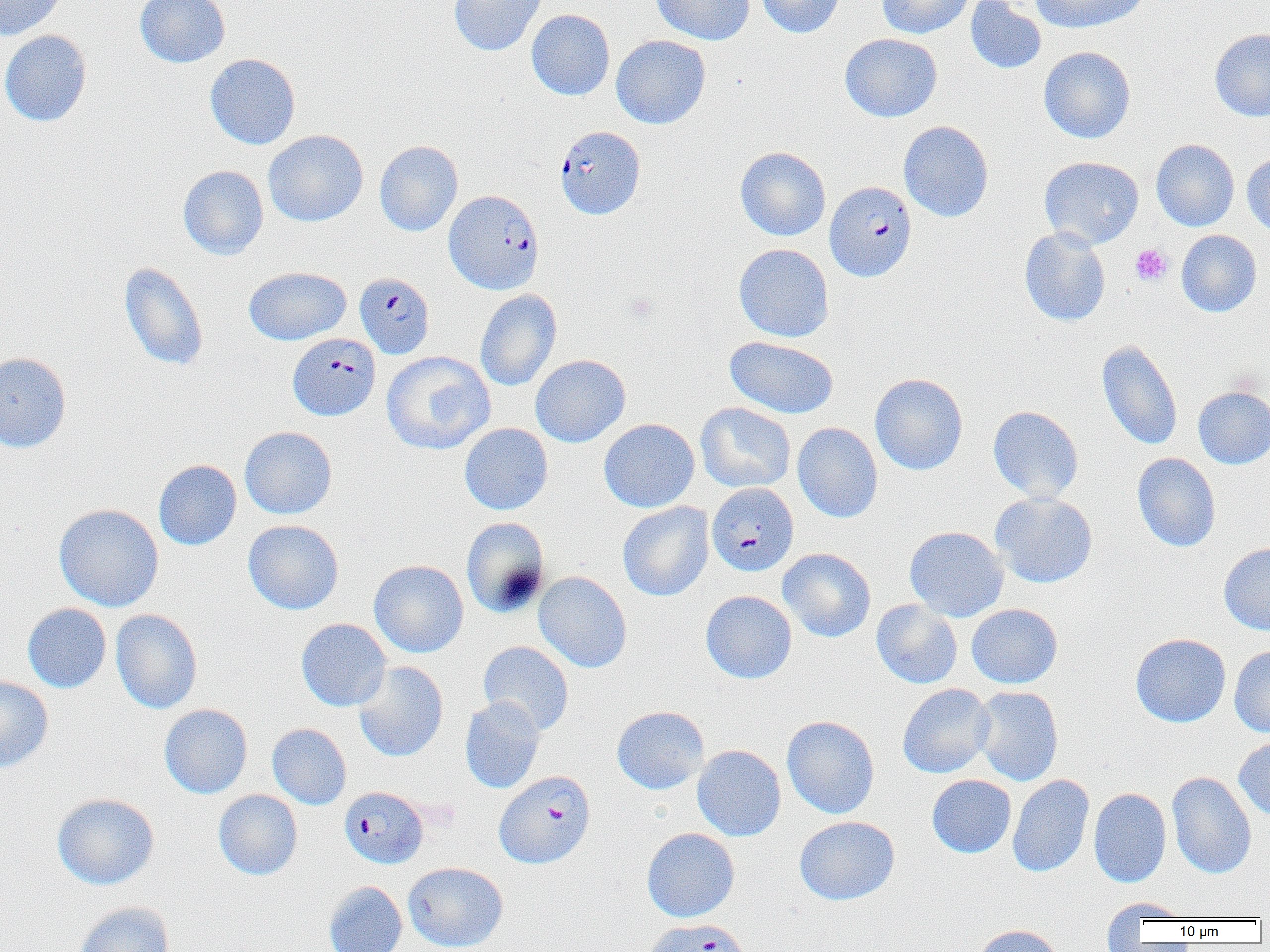

Approximate bounding boxes as [x1, y1, x2, y2] in pixels. Plasmodium falciparum-infected red blood cell locations: [555, 125, 645, 219], [825, 181, 917, 282], [445, 190, 544, 294], [354, 272, 435, 358], [288, 333, 380, 421], [707, 483, 798, 576], [494, 771, 596, 869], [339, 786, 428, 869], [641, 918, 754, 952]. Platelet locations: [1130, 244, 1172, 285]. Uninfected red blood cell locations: [0, 0, 67, 41], [135, 0, 230, 68], [448, 0, 546, 56], [651, 0, 755, 45], [756, 0, 845, 38], [876, 0, 975, 39], [965, 0, 1046, 75], [1030, 0, 1149, 33], [526, 9, 615, 101], [1210, 29, 1270, 121], [0, 30, 93, 127], [839, 33, 942, 122], [611, 35, 711, 129], [1038, 46, 1136, 144], [204, 53, 301, 150], [899, 121, 994, 222], [263, 129, 369, 227], [1151, 139, 1239, 231], [374, 140, 463, 236], [735, 146, 831, 241], [1242, 152, 1270, 237], [1039, 156, 1144, 249], [177, 165, 269, 260], [1019, 227, 1111, 326], [1176, 230, 1262, 317], [734, 243, 834, 342], [119, 262, 209, 371], [243, 267, 352, 345], [475, 289, 561, 391], [724, 335, 838, 418], [1096, 339, 1183, 450], [381, 351, 496, 455], [0, 352, 72, 452], [530, 355, 631, 447], [869, 373, 968, 474], [1193, 386, 1270, 469], [696, 402, 796, 492], [987, 405, 1084, 504], [598, 418, 699, 512], [792, 422, 883, 523], [459, 423, 553, 515], [239, 426, 338, 519], [1132, 452, 1221, 553], [153, 459, 241, 550], [990, 492, 1098, 588], [617, 501, 714, 601], [53, 503, 164, 612], [461, 517, 550, 618], [243, 519, 344, 615], [905, 526, 1008, 621], [1219, 543, 1270, 635], [778, 548, 876, 642], [369, 560, 469, 658], [533, 571, 632, 673], [700, 590, 797, 684], [871, 600, 963, 689], [22, 603, 111, 693], [966, 604, 1063, 688], [111, 609, 203, 713], [296, 618, 392, 711], [1130, 633, 1231, 727], [478, 640, 574, 735], [1229, 645, 1270, 737], [353, 661, 448, 762], [0, 675, 53, 773], [897, 683, 995, 778], [973, 685, 1063, 786], [460, 696, 546, 794], [159, 703, 253, 799], [611, 705, 709, 795], [781, 716, 880, 818], [267, 723, 351, 809], [1234, 735, 1270, 820], [692, 745, 786, 841], [1167, 771, 1257, 879], [927, 774, 1016, 858], [1007, 774, 1095, 878], [1089, 787, 1172, 887], [213, 789, 303, 880], [52, 792, 160, 889], [794, 815, 900, 905], [642, 828, 739, 922], [403, 862, 508, 951], [323, 881, 408, 952], [1101, 898, 1189, 929], [72, 901, 174, 952], [973, 924, 1064, 952]. Slide-level diagnosis: Plasmodium falciparum. Light microscopy. Thin blood smear. Image is 1270×952 pixels. One field of a larger specimen. 1000x magnification.